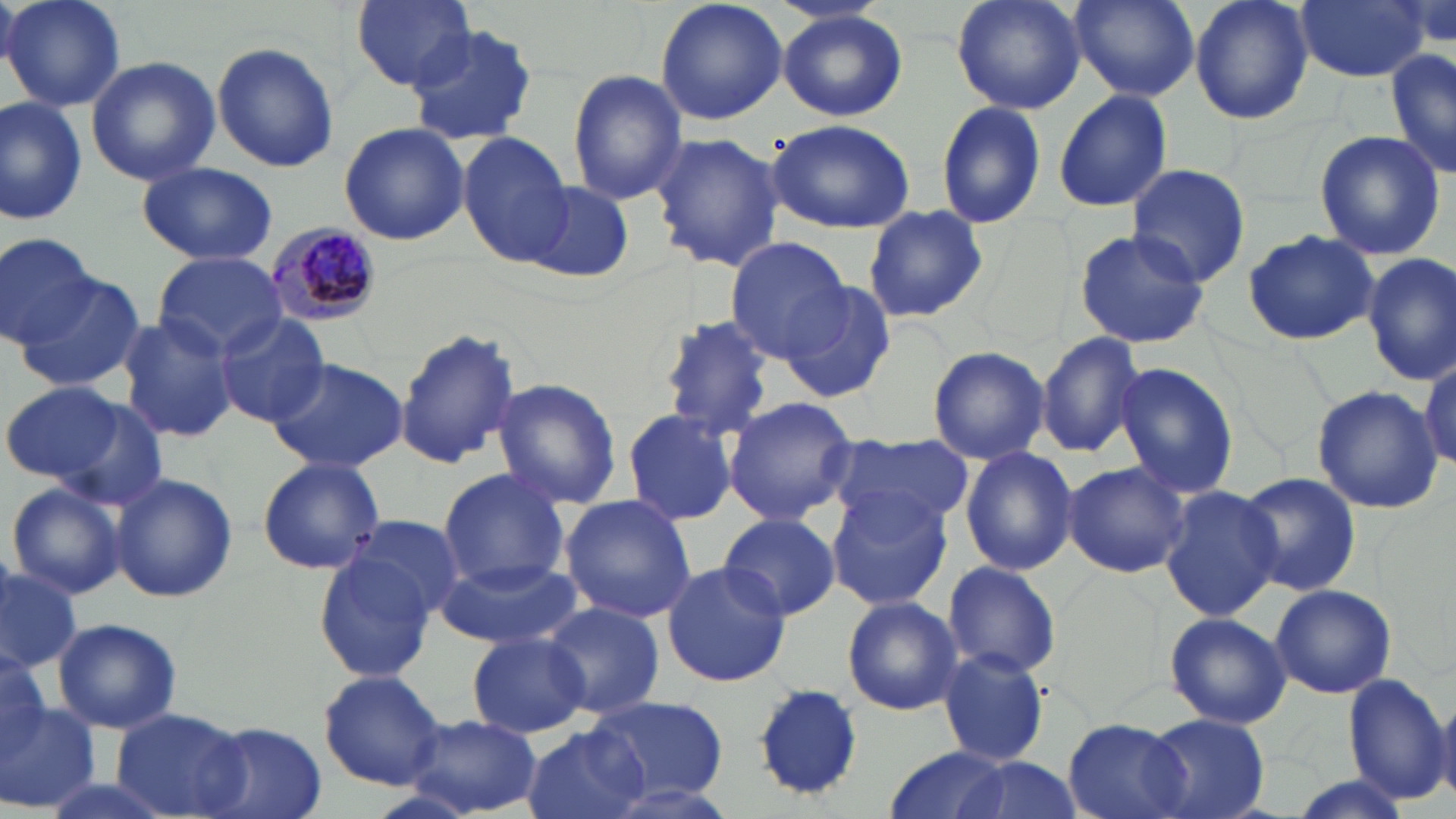
Approximate bounding boxes as (x1,y1)-(x2,y2) corner pairs in pixels. Plasmodium malariae-infected red blood cell locations: (261,222)-(383,329). Uninfected red blood cell locations: (4,0)-(126,112), (347,0)-(479,91), (655,0)-(787,125), (951,0)-(1086,116), (1068,0)-(1202,101), (1187,0)-(1314,125), (1293,0)-(1431,83), (777,9)-(908,122), (405,21)-(540,148), (212,41)-(342,175), (1386,49)-(1455,182), (85,57)-(220,186), (567,68)-(688,207), (1052,89)-(1173,213), (0,98)-(86,226), (934,98)-(1048,230), (767,118)-(915,233), (339,123)-(470,246), (1313,129)-(1445,261), (460,131)-(576,265), (650,131)-(784,273), (135,161)-(281,266), (1127,165)-(1251,287), (519,180)-(634,283), (864,207)-(988,323), (1072,229)-(1210,350), (1242,229)-(1381,347), (0,230)-(98,349), (725,238)-(853,361), (1364,252)-(1456,386), (154,253)-(290,358), (11,276)-(148,394), (779,278)-(898,403), (117,314)-(238,445), (214,314)-(331,429), (656,314)-(774,438), (395,328)-(521,471), (1036,331)-(1145,459), (927,346)-(1049,465), (1419,355)-(1454,469), (266,356)-(409,475), (1113,362)-(1239,501), (1,379)-(128,485), (490,379)-(622,509), (1311,386)-(1441,513), (33,393)-(169,508), (722,395)-(857,528), (622,409)-(739,526), (832,437)-(970,533), (961,445)-(1078,577), (257,457)-(384,575), (1061,462)-(1190,578), (437,468)-(571,590), (1239,471)-(1359,597), (110,472)-(238,604), (6,482)-(125,599), (1160,485)-(1282,622), (828,492)-(952,611), (559,494)-(697,622), (720,512)-(842,621), (344,513)-(467,625), (314,552)-(441,684), (435,558)-(584,649), (660,560)-(791,687), (942,561)-(1061,680), (1,566)-(82,671), (1271,583)-(1398,700), (841,596)-(961,715), (542,603)-(665,717), (1165,611)-(1291,729), (52,618)-(182,734), (466,633)-(590,738), (0,642)-(47,763), (937,650)-(1051,767), (318,669)-(447,789), (1340,671)-(1450,804), (750,682)-(867,804), (752,684)-(866,802), (582,695)-(731,802), (0,697)-(97,811), (113,707)-(250,818), (401,713)-(543,816), (1142,713)-(1270,819), (1062,717)-(1189,819), (196,723)-(328,819), (522,725)-(654,819), (881,744)-(1018,819), (943,755)-(1085,819), (1281,775)-(1415,819), (593,781)-(742,819). Slide-level diagnosis: Plasmodium malariae. Image is 1456×819 pixels. Thin blood smear. Optical microscopy. One field of a larger specimen. Captured at 1000x magnification. May-Grünwald-Giemsa-stained preparation.